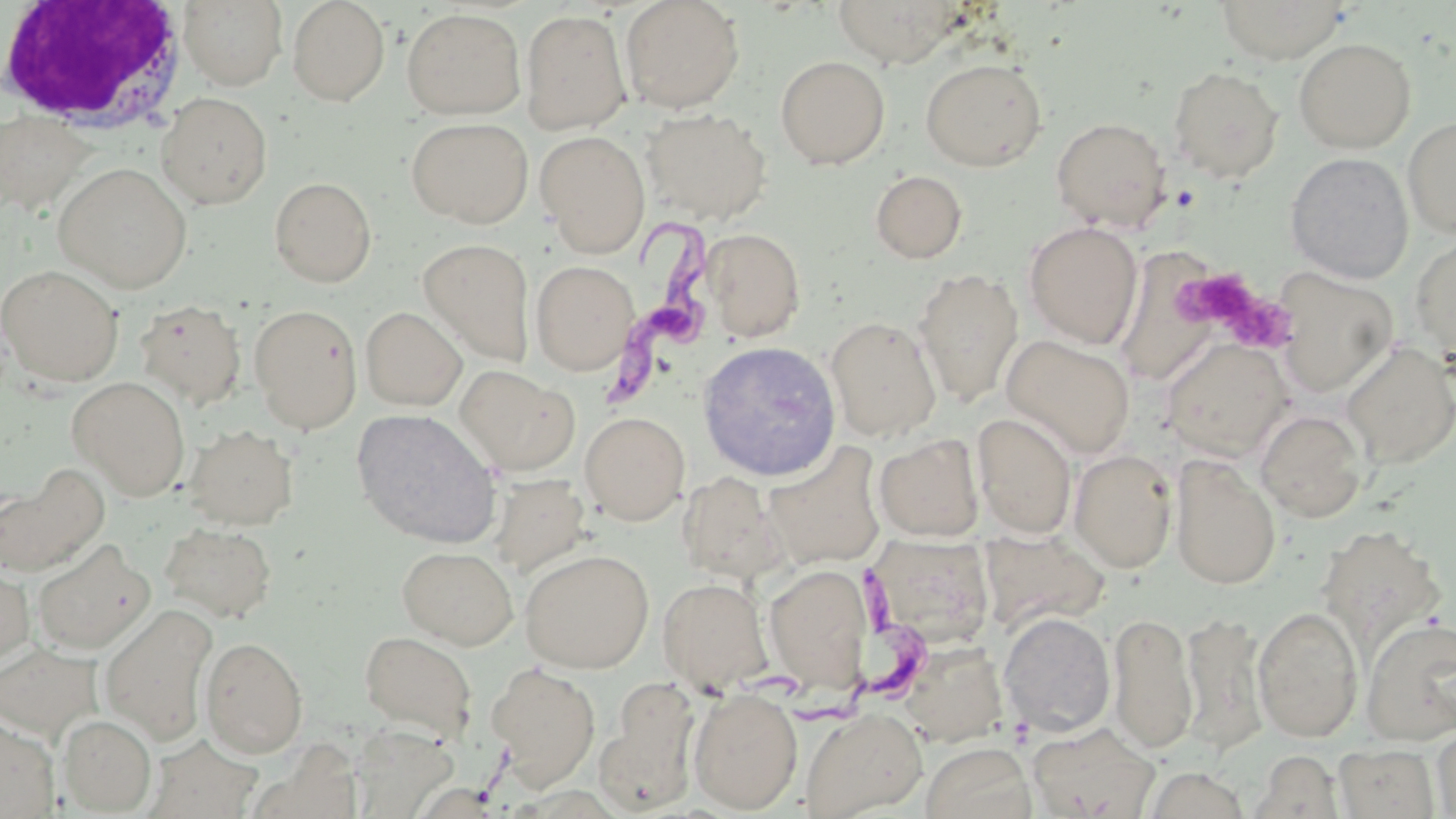
Summary:
  - Coordinate format: approximate bounding boxes as (x1,y1)-(x2,y2) corner pairs in pixels
  - Uninfected red blood cell locations: (178,0)-(287,90), (287,0)-(390,106), (620,0)-(746,113), (1214,0)-(1350,63), (831,1)-(968,67), (402,7)-(526,119), (521,9)-(632,134), (1293,37)-(1416,154), (775,55)-(890,169), (920,57)-(1047,171), (1167,65)-(1283,182), (156,92)-(273,209), (641,108)-(773,224), (1,112)-(92,214), (1402,115)-(1456,238), (406,117)-(532,228), (1051,117)-(1172,232), (534,130)-(651,256), (1284,152)-(1414,283), (54,162)-(192,292), (870,169)-(968,263), (269,177)-(376,287), (1024,221)-(1143,348), (700,228)-(806,342), (1409,232)-(1456,365), (418,239)-(535,366), (1114,246)-(1228,400), (530,260)-(638,375), (0,264)-(124,386), (1275,267)-(1399,397), (913,268)-(1024,407), (134,299)-(247,411), (248,304)-(363,433), (361,307)-(467,411), (825,316)-(942,441), (1001,334)-(1136,459), (1160,337)-(1293,461), (703,341)-(841,486), (1341,341)-(1456,468), (456,366)-(577,474), (68,376)-(190,499), (351,408)-(503,548), (1255,409)-(1367,523), (580,412)-(689,525), (973,413)-(1077,539), (184,424)-(298,529), (874,434)-(985,542), (763,443)-(887,570), (1069,448)-(1178,573), (1169,453)-(1281,589), (1,468)-(107,576), (678,471)-(788,585), (487,473)-(591,576), (160,522)-(277,623), (1315,524)-(1446,658), (32,541)-(155,654), (397,545)-(518,649), (519,548)-(654,673), (764,563)-(872,692), (0,564)-(34,666), (658,578)-(772,691), (101,604)-(217,745), (1252,606)-(1363,742), (1108,610)-(1198,754), (999,611)-(1116,737), (1181,611)-(1268,754), (1361,617)-(1456,744), (360,630)-(477,739), (200,636)-(308,758), (902,641)-(1007,747), (0,644)-(102,742), (486,662)-(601,788), (597,677)-(701,814), (688,687)-(803,813), (802,707)-(928,818), (58,715)-(156,814), (0,716)-(60,818), (1028,723)-(1160,819), (1432,724)-(1456,817), (351,725)-(458,817), (146,734)-(263,819), (921,742)-(1036,819), (1333,742)-(1439,818), (1251,750)-(1345,818), (1143,766)-(1251,819)
  - Platelet locations: (1176,267)-(1288,346)
  - White blood cell locations: (0,3)-(190,138)
  - Trypanosoma brucei locations: (595,216)-(720,412), (798,565)-(930,722)
  - Slide-level diagnosis: Trypanosoma brucei
  - Image size: 1456×819 pixels
  - Modality: light microscopy
  - Stain: May-Grünwald-Giemsa
  - Magnification: 1000x
  - Field of view: one of a larger specimen
  - Preparation: thin blood film